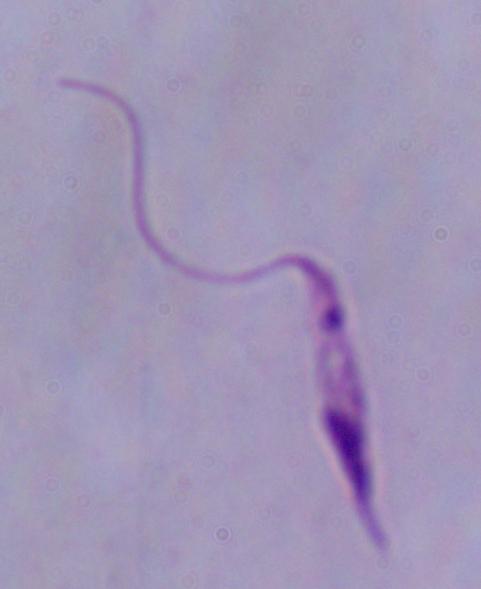
{
  "modality": "photomicrograph",
  "magnification": "1000x",
  "identification": "Leishmania"
}